Assess this cell for malaria.
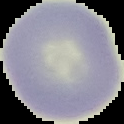
Uninfected.

Summary:
  - Image type: segmented cell region on a black background
  - Image size: 124×124 pixels
  - Preparation: thin blood smear